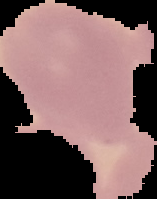

Malaria status: uninfected. From a thin blood smear. Cell region segmented out of the field of view; the surrounding area is masked to black. Image is 157×199 pixels.